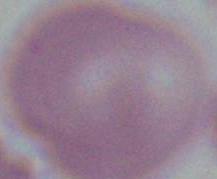 A red blood cell is seen. Photomicrograph. Captured at 1000x magnification.